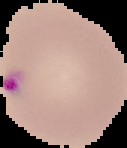

Summary:
  - Image size: 127×148 pixels
  - Image type: cell region segmented out of the field of view; surrounding area masked to black
  - Preparation: thin blood smear
  - Malaria status: parasitized